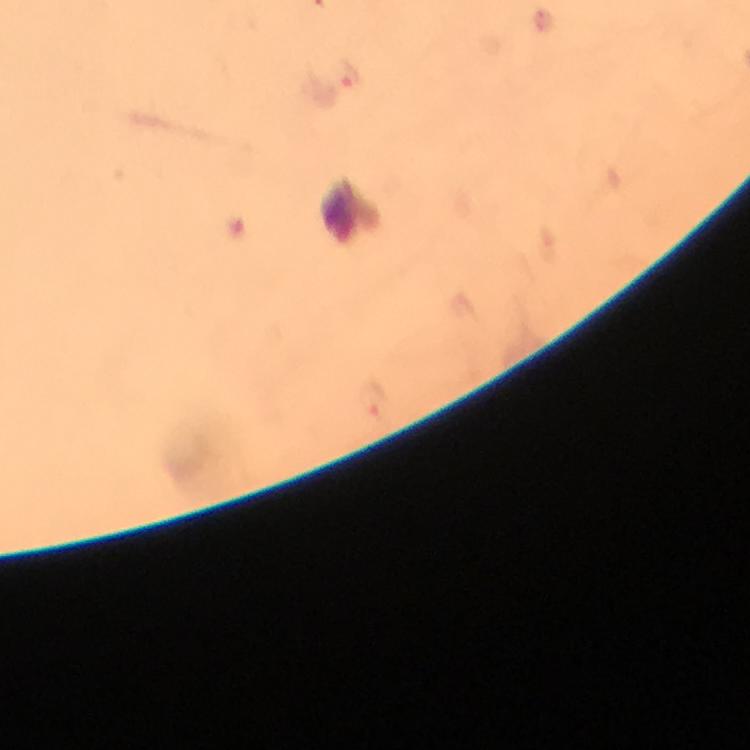
Approximate centers as (x, y) in pixels. Malaria parasite locations: (350, 74). Immersion oil was used. Giemsa stain. Image is 750×750 pixels. Photographed through the microscope with a smartphone camera. From a malaria diagnostic workup. Thick smear. At 100x magnification. A crop from one field of view.